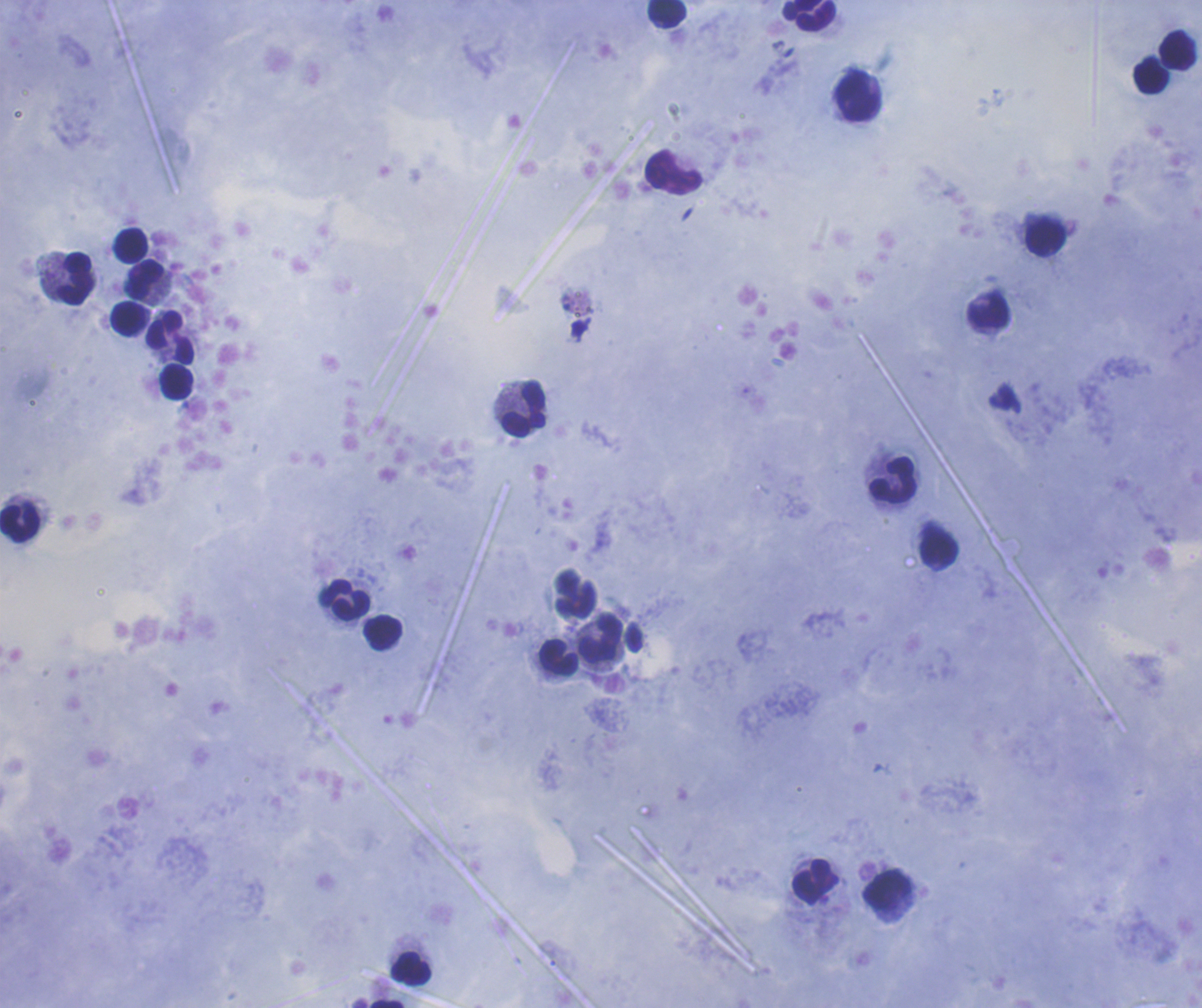 Approximate centers as (x, y) in pixels. Leukocyte locations: (667, 13), (809, 16), (1178, 51), (1151, 74), (857, 97), (673, 172), (1046, 237), (132, 245), (75, 279), (145, 280), (988, 311), (130, 319), (171, 338), (176, 382), (525, 408), (893, 480), (20, 523), (938, 550), (345, 600), (382, 633), (601, 639), (559, 658), (815, 882), (887, 890), (411, 969), (387, 1004). Result: negative for Plasmodium parasites. Coloration quality: good. Captured at 100x magnification. Image is 1202×1008 pixels. Thick smear of blood. Previously used in a real diagnosis. Background quality: good. Romanowsky stain. Single field of view.